Assess for Plasmodium parasites.
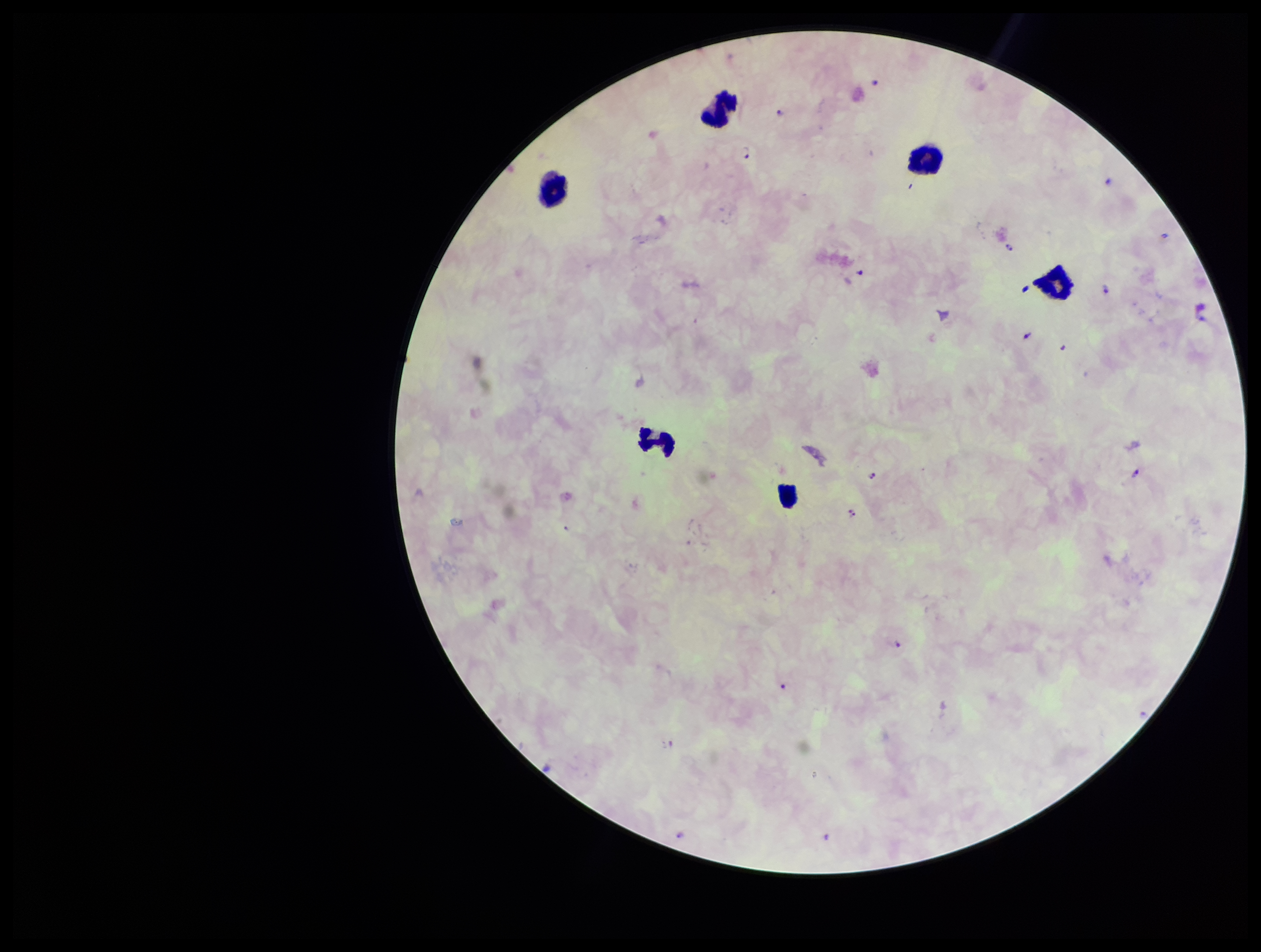

Detected.

leukocyte count = 6
parasite count = 15
stain = Giemsa
field of view = one from this slide
preparation = thick smear
image size = 1261×952 pixels
species reported for this patient = Plasmodium falciparum
capture = smartphone photograph through the microscope eyepiece
patient malaria status = positive